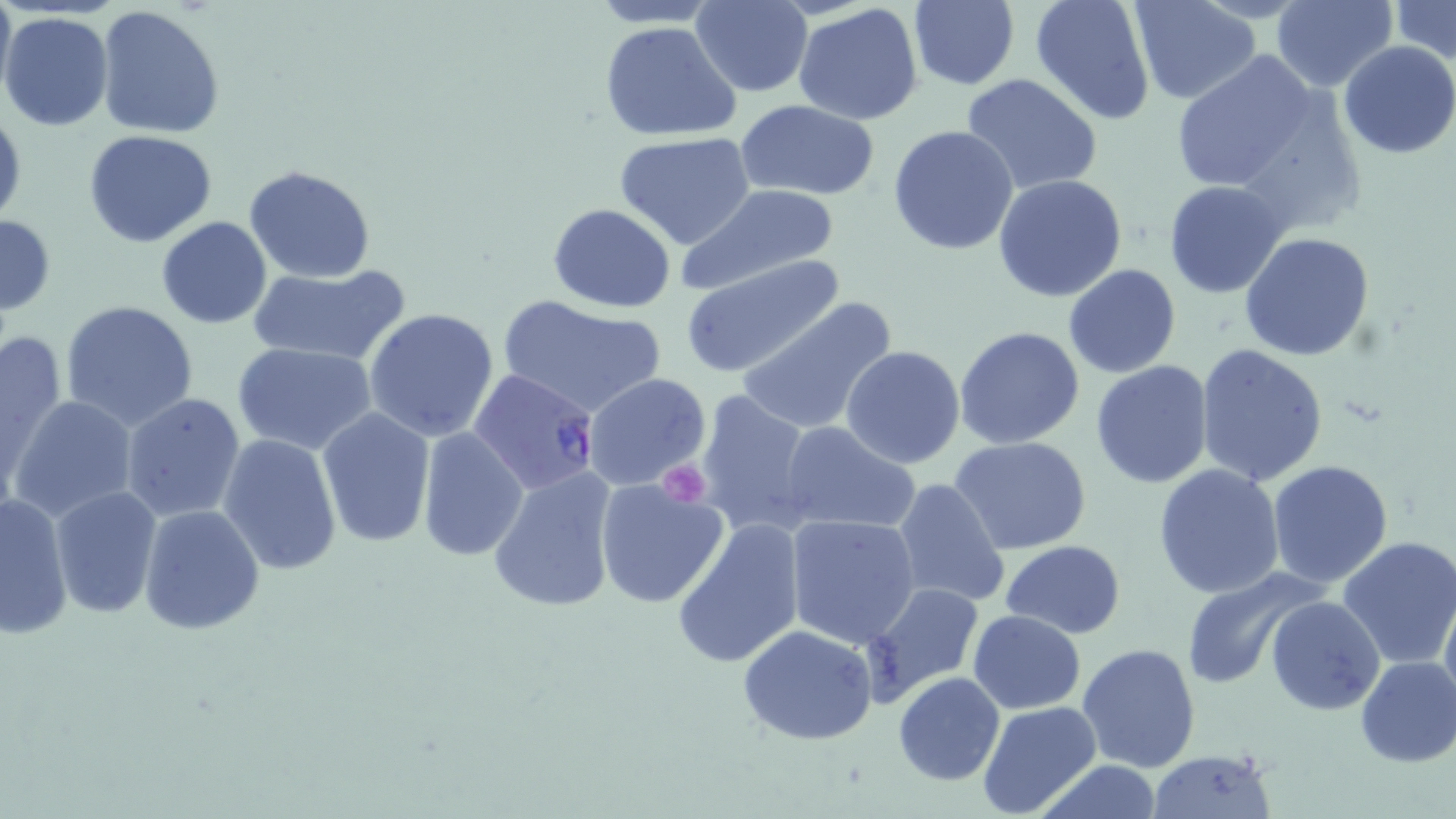

slide-level diagnosis = Plasmodium falciparum
uninfected red blood cell locations = approximate bounding boxes as (x1, y1, x2, y2) in pixels: (0, 0, 15, 102), (587, 0, 723, 27), (1028, 0, 1158, 125), (1391, 0, 1456, 65), (691, 1, 814, 97), (906, 1, 1021, 89), (1129, 1, 1261, 104), (1270, 1, 1396, 90), (794, 3, 924, 126), (96, 4, 225, 141), (1, 11, 115, 131), (598, 20, 740, 142), (1337, 41, 1456, 159), (1170, 48, 1331, 198), (960, 73, 1102, 197), (737, 101, 883, 199), (0, 104, 24, 230), (888, 124, 1021, 255), (84, 128, 218, 246), (612, 132, 756, 249), (245, 166, 375, 282), (993, 173, 1128, 304), (1163, 181, 1289, 297), (678, 184, 841, 292), (547, 203, 676, 313), (0, 214, 56, 319), (156, 217, 271, 329), (1239, 232, 1375, 361), (679, 254, 846, 379), (246, 262, 412, 367), (1063, 265, 1181, 379), (498, 296, 667, 418), (736, 297, 897, 437), (60, 300, 201, 431), (363, 308, 501, 444), (955, 325, 1085, 450), (0, 326, 69, 483), (233, 343, 377, 456), (841, 345, 965, 468), (1194, 345, 1330, 488), (1089, 361, 1215, 487), (584, 374, 712, 492), (694, 389, 819, 538), (120, 393, 247, 524), (8, 396, 139, 522), (316, 407, 435, 547), (778, 421, 919, 535), (417, 427, 527, 560), (217, 433, 343, 576), (950, 436, 1092, 555), (1266, 460, 1396, 588), (1154, 463, 1285, 599), (486, 467, 620, 615), (891, 477, 1011, 609), (593, 478, 730, 610), (49, 484, 161, 620), (0, 492, 73, 638), (138, 505, 263, 636), (786, 514, 921, 649), (671, 518, 806, 669), (1335, 536, 1456, 671), (1000, 540, 1128, 637), (1179, 565, 1325, 689), (861, 583, 984, 708), (1439, 585, 1456, 716), (1265, 596, 1384, 714), (969, 610, 1086, 712), (737, 625, 879, 747), (1078, 642, 1201, 770), (1355, 656, 1456, 769), (894, 673, 1006, 786), (977, 701, 1103, 819), (1144, 750, 1277, 819), (1033, 760, 1165, 818)
preparation = thin blood film
magnification = 1000x
field of view = single
platelet locations = approximate bounding boxes as (x1, y1, x2, y2) in pixels: (656, 462, 709, 505)
modality = light microscopy
image size = 1456×819 pixels
stain = May-Grünwald-Giemsa
Plasmodium falciparum-infected red blood cell locations = approximate bounding boxes as (x1, y1, x2, y2) in pixels: (469, 367, 602, 497)